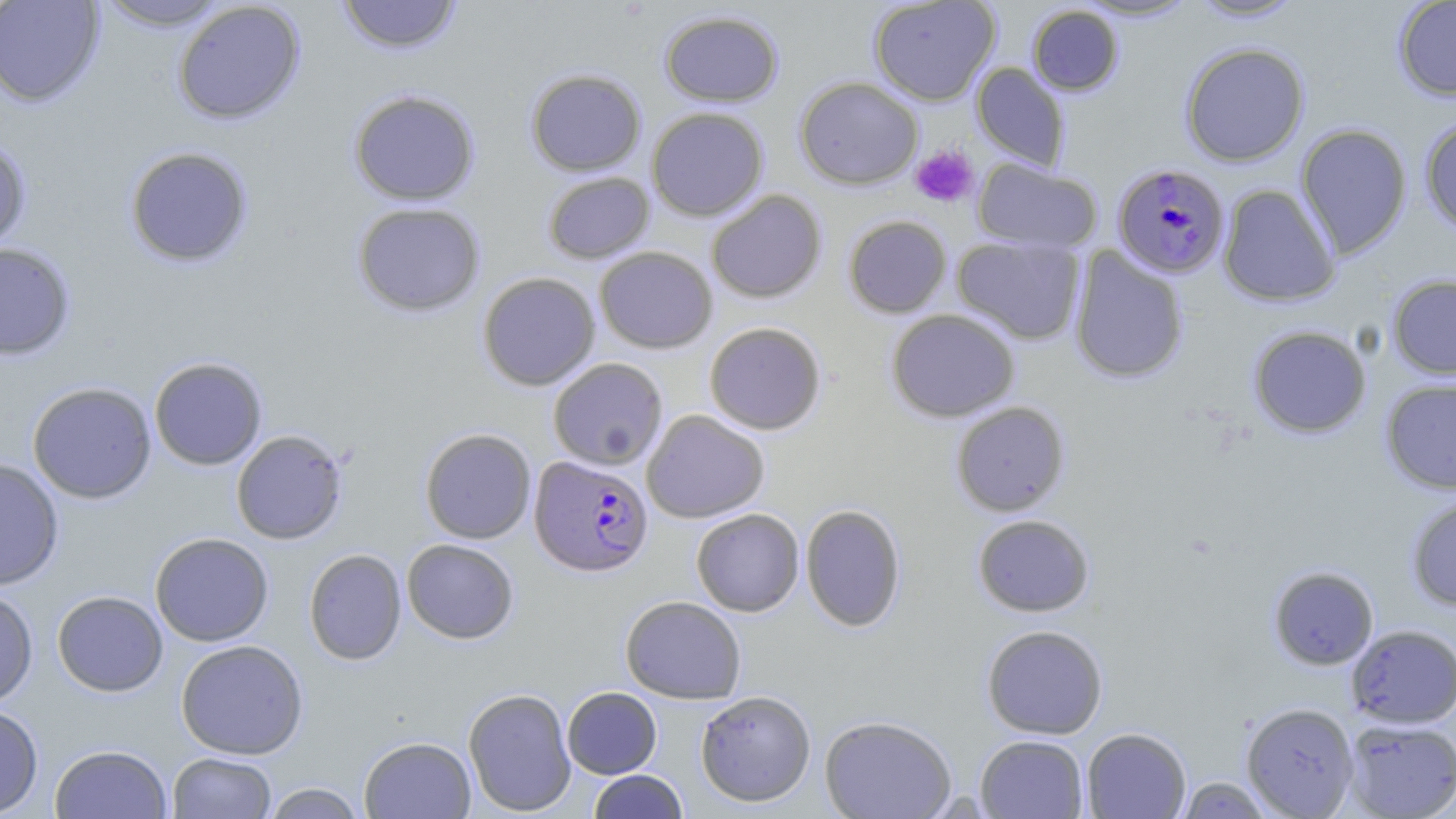

Summary:
  - Coordinate format: approximate bounding boxes as named x1/y1/x2/y2 corners in pixels
  - Plasmodium falciparum-infected red blood cell locations: (x1=1112, y1=163, x2=1231, y2=279), (x1=529, y1=456, x2=654, y2=577)
  - Platelet locations: (x1=910, y1=144, x2=979, y2=207)
  - Uninfected red blood cell locations: (x1=0, y1=0, x2=105, y2=108), (x1=335, y1=0, x2=463, y2=54), (x1=868, y1=0, x2=1001, y2=106), (x1=1074, y1=0, x2=1198, y2=21), (x1=1188, y1=0, x2=1305, y2=22), (x1=1393, y1=0, x2=1456, y2=101), (x1=93, y1=1, x2=235, y2=31), (x1=172, y1=1, x2=306, y2=125), (x1=1027, y1=4, x2=1124, y2=96), (x1=659, y1=10, x2=783, y2=107), (x1=1180, y1=42, x2=1309, y2=166), (x1=971, y1=62, x2=1070, y2=172), (x1=525, y1=68, x2=646, y2=176), (x1=794, y1=76, x2=923, y2=190), (x1=348, y1=88, x2=481, y2=206), (x1=646, y1=107, x2=769, y2=221), (x1=1419, y1=117, x2=1456, y2=234), (x1=1295, y1=124, x2=1412, y2=260), (x1=0, y1=137, x2=32, y2=254), (x1=124, y1=146, x2=254, y2=268), (x1=973, y1=159, x2=1102, y2=253), (x1=542, y1=171, x2=655, y2=264), (x1=1218, y1=183, x2=1340, y2=307), (x1=706, y1=190, x2=827, y2=304), (x1=351, y1=202, x2=486, y2=317), (x1=843, y1=215, x2=952, y2=318), (x1=951, y1=235, x2=1085, y2=344), (x1=0, y1=242, x2=76, y2=361), (x1=1068, y1=245, x2=1189, y2=384), (x1=594, y1=247, x2=718, y2=354), (x1=477, y1=272, x2=601, y2=391), (x1=1387, y1=273, x2=1456, y2=379), (x1=886, y1=309, x2=1019, y2=422), (x1=704, y1=321, x2=826, y2=435), (x1=1248, y1=325, x2=1372, y2=438), (x1=149, y1=356, x2=268, y2=470), (x1=547, y1=357, x2=668, y2=469), (x1=1380, y1=378, x2=1456, y2=494), (x1=27, y1=382, x2=157, y2=503), (x1=950, y1=401, x2=1070, y2=516), (x1=641, y1=410, x2=770, y2=523), (x1=419, y1=428, x2=536, y2=544), (x1=230, y1=429, x2=348, y2=544), (x1=0, y1=458, x2=64, y2=591), (x1=1405, y1=493, x2=1456, y2=611), (x1=800, y1=503, x2=907, y2=632), (x1=691, y1=508, x2=805, y2=616), (x1=972, y1=514, x2=1095, y2=617), (x1=149, y1=532, x2=274, y2=647), (x1=402, y1=538, x2=519, y2=644), (x1=304, y1=548, x2=407, y2=666), (x1=1268, y1=565, x2=1379, y2=670), (x1=0, y1=588, x2=38, y2=708), (x1=52, y1=590, x2=168, y2=696), (x1=620, y1=595, x2=747, y2=704), (x1=981, y1=624, x2=1108, y2=739), (x1=1346, y1=625, x2=1456, y2=728), (x1=175, y1=639, x2=308, y2=759), (x1=562, y1=686, x2=662, y2=778), (x1=462, y1=687, x2=577, y2=816), (x1=695, y1=691, x2=816, y2=807), (x1=1241, y1=702, x2=1359, y2=817), (x1=0, y1=704, x2=43, y2=817), (x1=819, y1=714, x2=957, y2=819), (x1=1342, y1=717, x2=1456, y2=818), (x1=1081, y1=727, x2=1191, y2=818), (x1=975, y1=734, x2=1089, y2=818), (x1=359, y1=735, x2=476, y2=818), (x1=49, y1=744, x2=172, y2=818), (x1=167, y1=752, x2=276, y2=818), (x1=588, y1=770, x2=688, y2=818), (x1=1174, y1=776, x2=1275, y2=818), (x1=261, y1=782, x2=366, y2=818)
  - Slide-level diagnosis: Plasmodium falciparum
  - Preparation: thin blood smear
  - Magnification: 1000x
  - Stain: May-Grünwald-Giemsa
  - Field of view: single
  - Image size: 1456×819 pixels
  - Modality: light microscopy